Assess this cell for malaria.
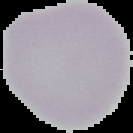
Uninfected.

{
  "image_type": "segmented cell region with the area outside set to black",
  "image_size": "133×133 pixels",
  "preparation": "thin blood film"
}